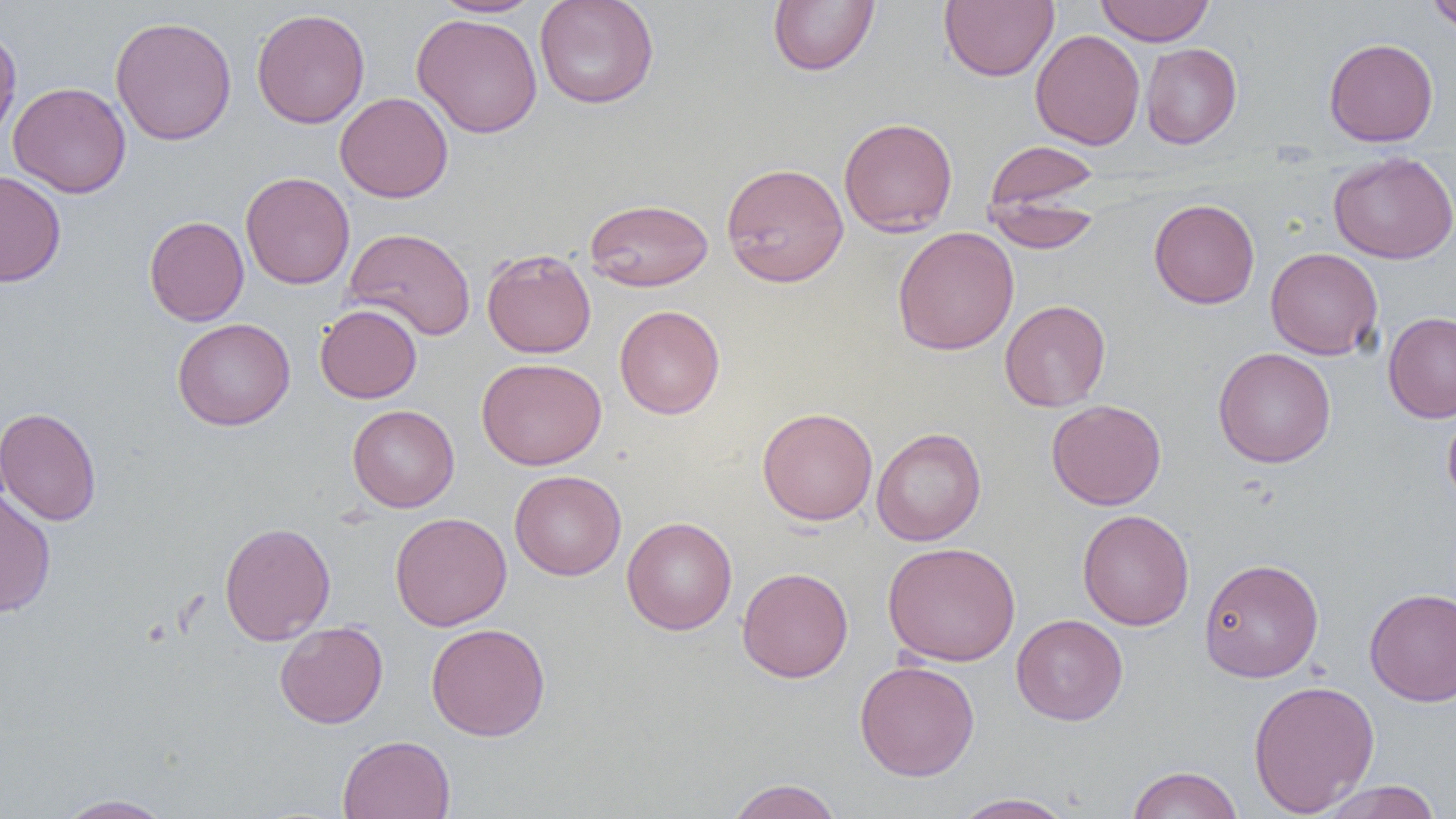
Summary:
  - Coordinate format: approximate bounding boxes as (x1,y1)-(x2,y2) corner pairs in pixels
  - Uninfected red blood cell locations: (534,0)-(659,109), (767,0)-(880,76), (940,0)-(1058,82), (1096,0)-(1215,45), (1425,0)-(1456,34), (432,1)-(542,18), (251,8)-(370,128), (411,13)-(543,138), (110,16)-(237,146), (0,26)-(22,145), (1030,29)-(1145,150), (1324,38)-(1438,147), (1140,43)-(1242,148), (8,82)-(131,198), (334,92)-(453,203), (838,116)-(958,236), (984,140)-(1101,218), (1328,151)-(1456,264), (721,162)-(849,288), (0,170)-(66,287), (241,172)-(355,289), (986,194)-(1102,253), (584,198)-(714,292), (1148,198)-(1260,309), (144,215)-(249,326), (344,227)-(476,341), (892,227)-(1019,355), (1265,247)-(1383,360), (481,248)-(596,358), (999,299)-(1111,411), (315,304)-(422,403), (614,305)-(725,419), (1383,311)-(1456,424), (172,317)-(295,430), (1213,347)-(1336,468), (477,357)-(607,470), (1046,399)-(1167,510), (347,404)-(459,512), (1443,404)-(1456,512), (0,407)-(102,526), (757,407)-(878,525), (871,427)-(986,546), (509,470)-(626,581), (0,488)-(57,618), (1078,509)-(1194,631), (390,513)-(512,631), (622,516)-(737,635), (219,522)-(336,645), (882,541)-(1021,666), (1198,557)-(1324,683), (738,567)-(854,682), (1364,588)-(1456,707), (1011,614)-(1128,725), (275,621)-(388,728), (426,623)-(551,741), (854,660)-(980,780), (1248,679)-(1380,816), (337,734)-(455,819), (1126,765)-(1243,819), (725,779)-(843,819), (1317,780)-(1443,818), (949,792)-(1079,819), (54,793)-(177,818)
  - Slide-level diagnosis: negative for blood parasites
  - Magnification: 1000x
  - Field of view: one of a larger specimen
  - Modality: optical microscopy
  - Image size: 1456×819 pixels
  - Preparation: thin blood film